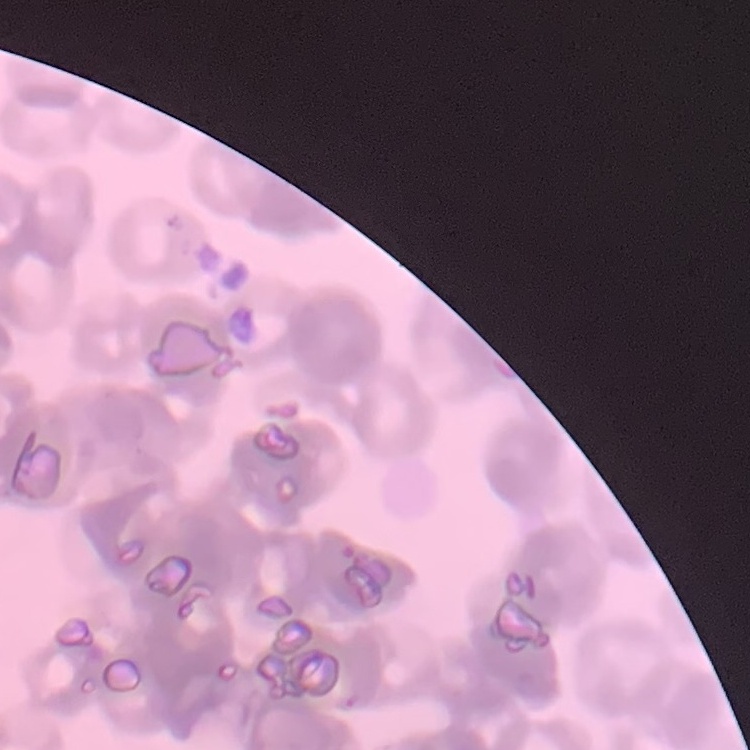
red_blood_cell_morphology: rouleaux formation
image_type: square crop of a larger photomicrograph
preparation: thin blood smear
stain: Field's or Giemsa